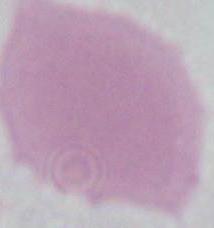
Summary:
  - Identification: red blood cell
  - Magnification: 1000x
  - Modality: photomicrograph